Describe the morphology of the red blood cells.
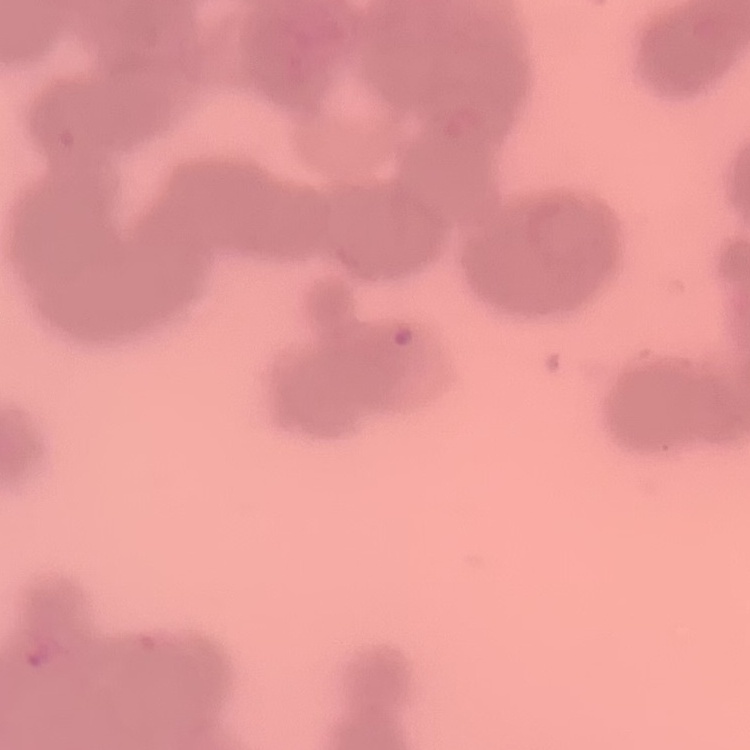

Rouleaux formation.

Stained with either Field's or Giemsa. Square crop of a larger photomicrograph. Thin peripheral smear.